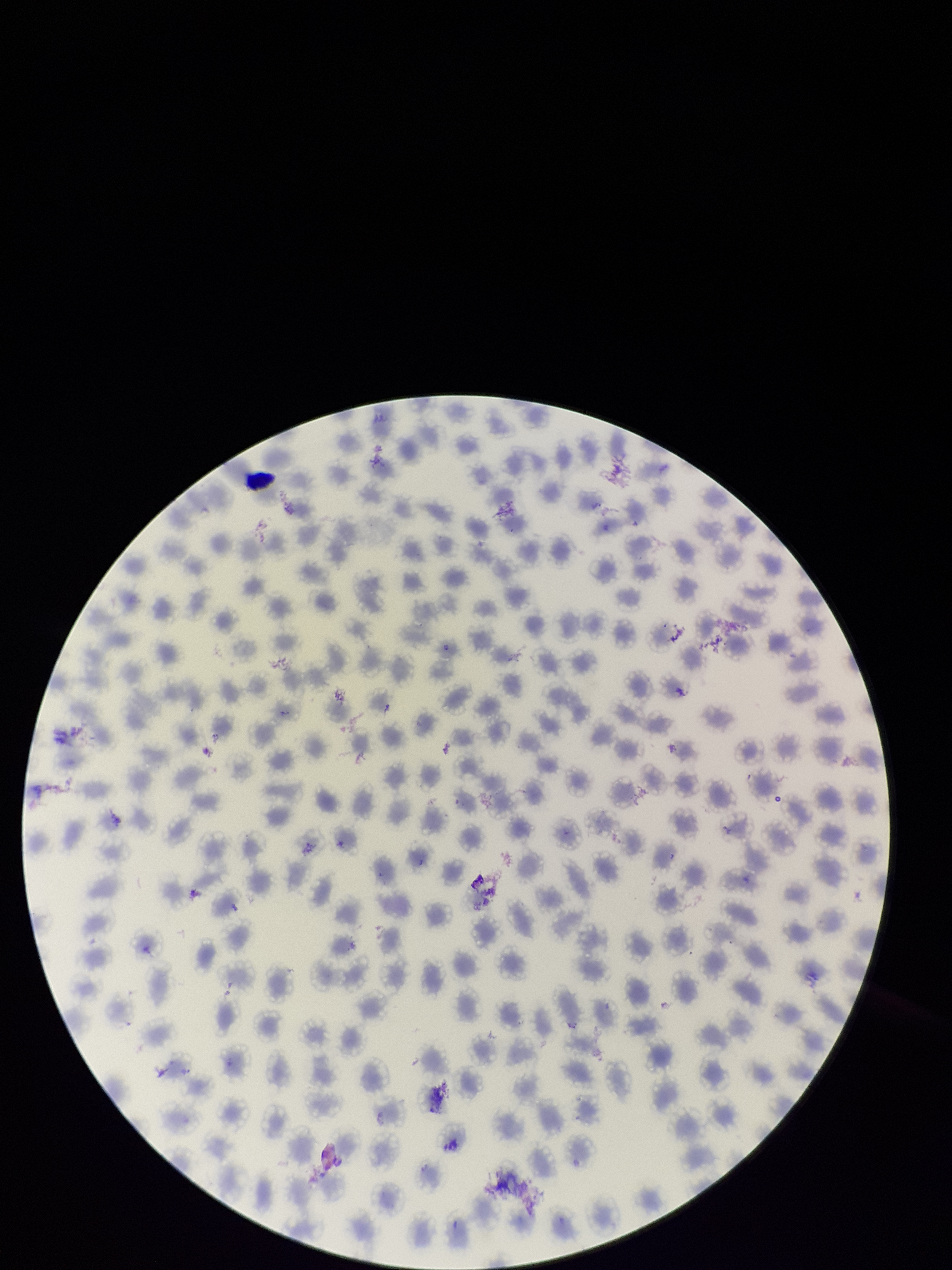

capture = smartphone photograph through the microscope eyepiece
stain = Giemsa
red blood cell count = 239
parasitized red blood cells = none detected
image size = 952×1270 pixels
parasitized red blood cell count = 0
field of view = single
species reported for this patient = Plasmodium vivax
patient malaria status = infected
preparation = thin blood smear